Comment on the morphology of the erythrocytes.
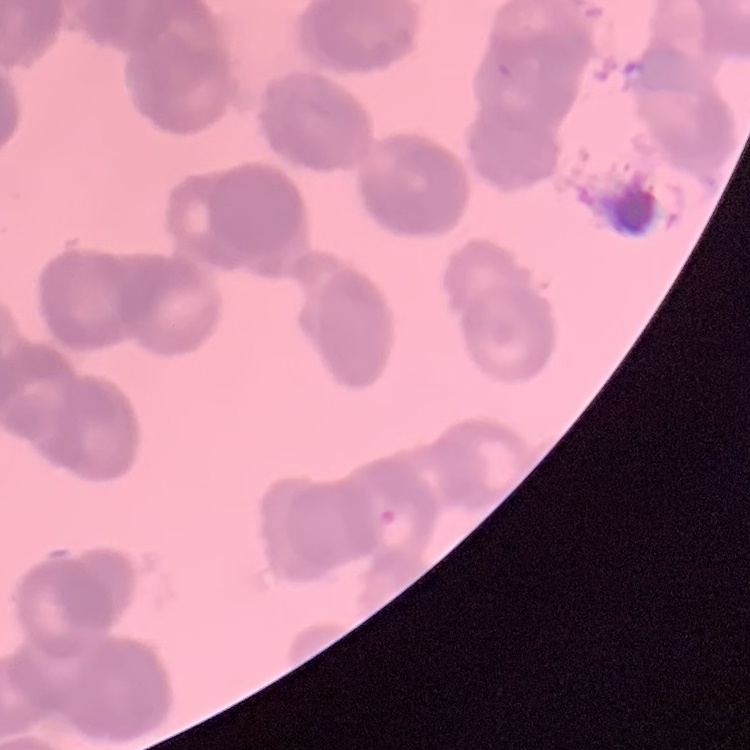
Rouleaux formation.

Square crop of a larger photomicrograph. Field's or Giemsa stain. Thin peripheral smear.